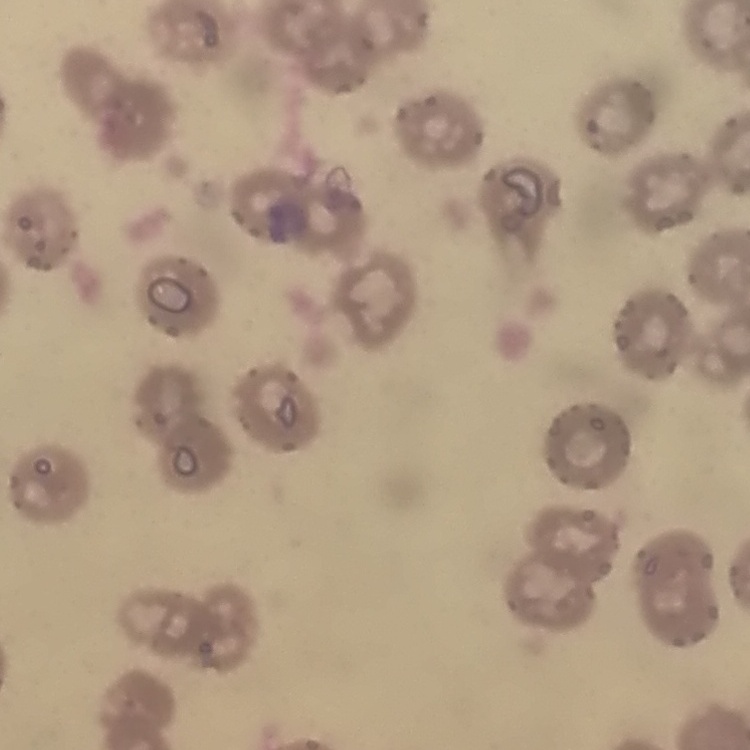

Summary:
  - Red blood cell morphology: no rouleaux formation
  - Preparation: thin blood film
  - Image type: one tile cut from a larger photomicrograph
  - Stain: Field's or Giemsa